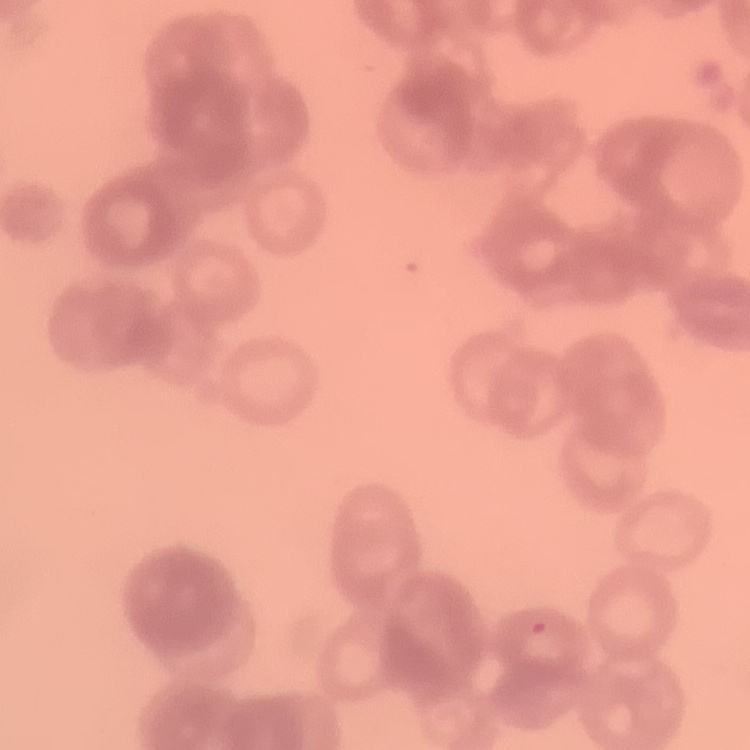
erythrocyte morphology = rouleaux formation
preparation = thin peripheral smear
image type = one tile cut from a larger photomicrograph
stain = Field's or Giemsa